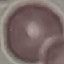
result = negative for malaria parasites
stain = Giemsa
capture = smartphone through the microscope eyepiece
preparation = thin smear
image type = cell patch, automatically extracted from a larger field of view and resized to 64 × 64 pixels